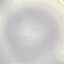

result = no malaria parasites seen
stain = Giemsa
preparation = thin smear
image type = automatically extracted cell patch, resized to 64 × 64 pixels
capture = smartphone through the microscope eyepiece